Locate every leukocyte (white blood cell).
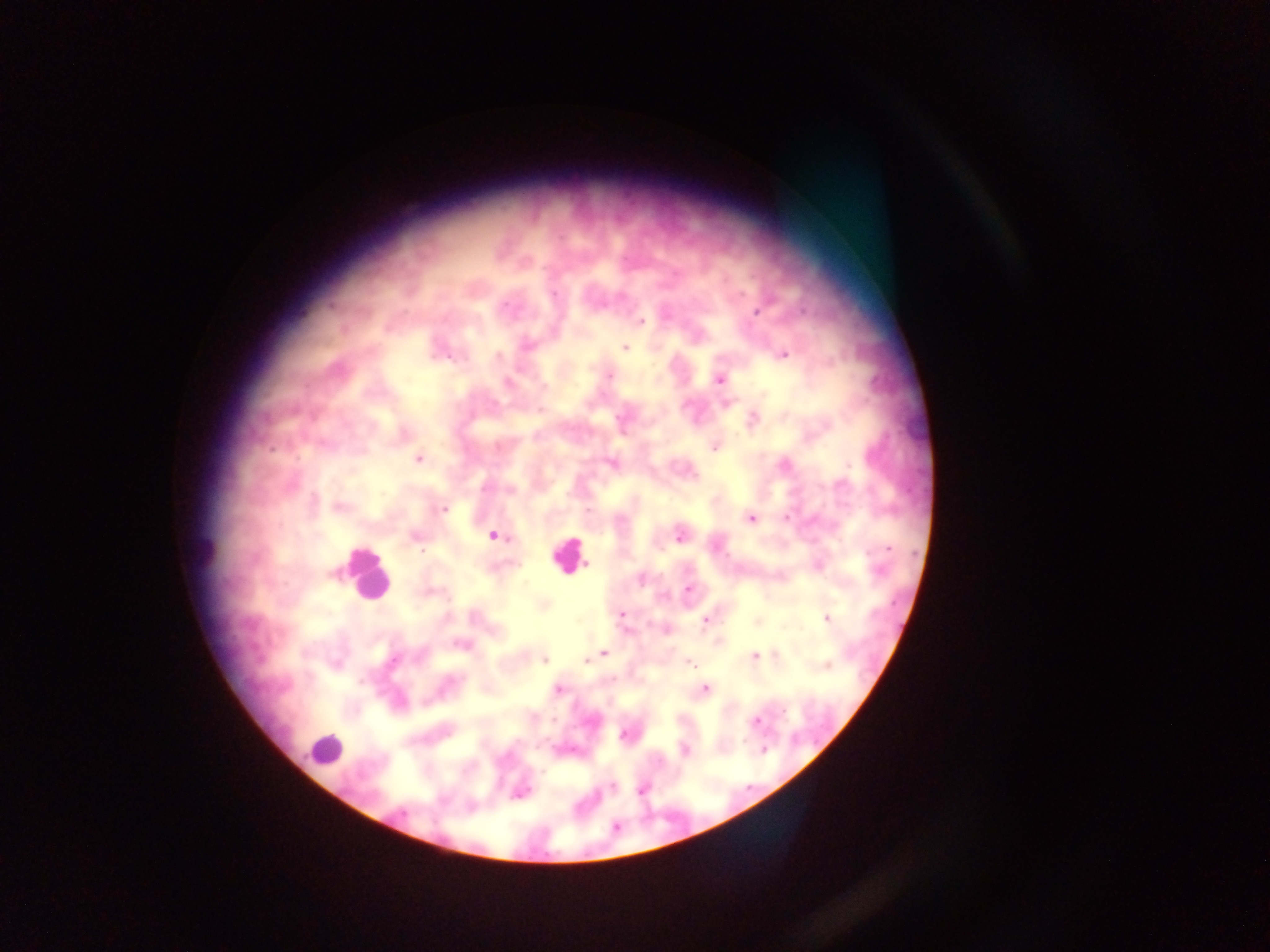

Approximate centers as [x, y] in pixels.
Leukocytes: [206, 554], [567, 554], [366, 574], [325, 749].

Summary:
  - Plasmodium parasite locations: [756, 311], [641, 322], [525, 344], [625, 347], [783, 354], [608, 376], [719, 379], [507, 383], [726, 402], [783, 416], [752, 420], [714, 445], [418, 458], [611, 463], [783, 464], [338, 506], [444, 509], [750, 518], [413, 535], [493, 535], [679, 535], [818, 565], [687, 589], [543, 605], [474, 614], [622, 614], [827, 617], [705, 619], [757, 621], [665, 629], [718, 641], [460, 645], [603, 653], [774, 655], [597, 656], [754, 656], [544, 659], [583, 660], [687, 662], [825, 665], [557, 689], [704, 689], [755, 720], [627, 734], [684, 750], [764, 750], [611, 787], [641, 789], [519, 791], [616, 827]
  - Preparation: thick blood smear
  - Country: Ghana
  - Image size: 1270×952 pixels
  - Capture: mobile-phone photograph through a microscope
  - Field of view: single